State which parasite is depicted.
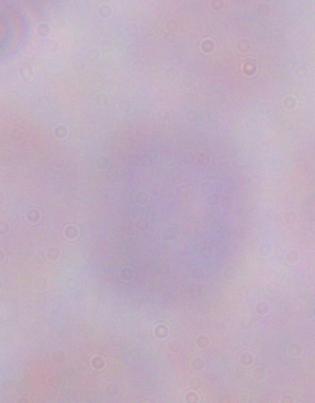
This is a trypanosome.

Summary:
  - Modality: photomicrograph
  - Magnification: 1000x